Name the cell type shown.
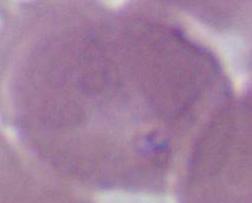
An erythrocyte.

Photomicrograph. Captured at 1000x magnification.